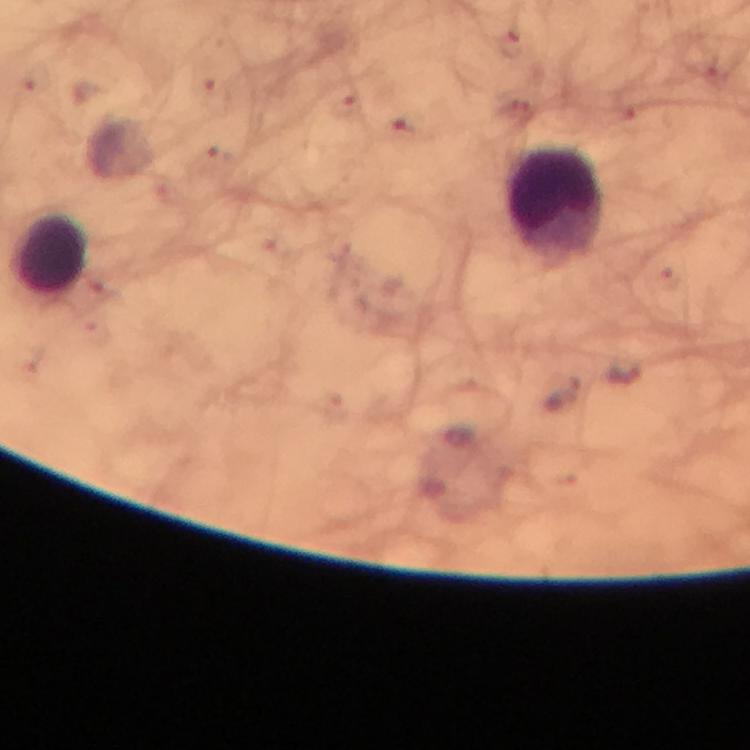

Approximate centers as (x, y) in pixels. Leukocyte locations: (556, 203), (49, 251). A crop from one field of view. Giemsa-stained preparation. Immersion oil applied. Smartphone photograph taken through a microscope. Plasmodium parasites: none seen. 100x magnification. Image is 750×750 pixels. Thick blood film. From a malaria diagnostic workup.